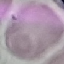
Summary:
  - Malaria status: uninfected
  - Preparation: thin blood film
  - Image type: automatically extracted cell patch, resized to 64 × 64 pixels
  - Stain: Giemsa
  - Capture: smartphone camera at the microscope eyepiece